Comment on the morphology of the erythrocytes.
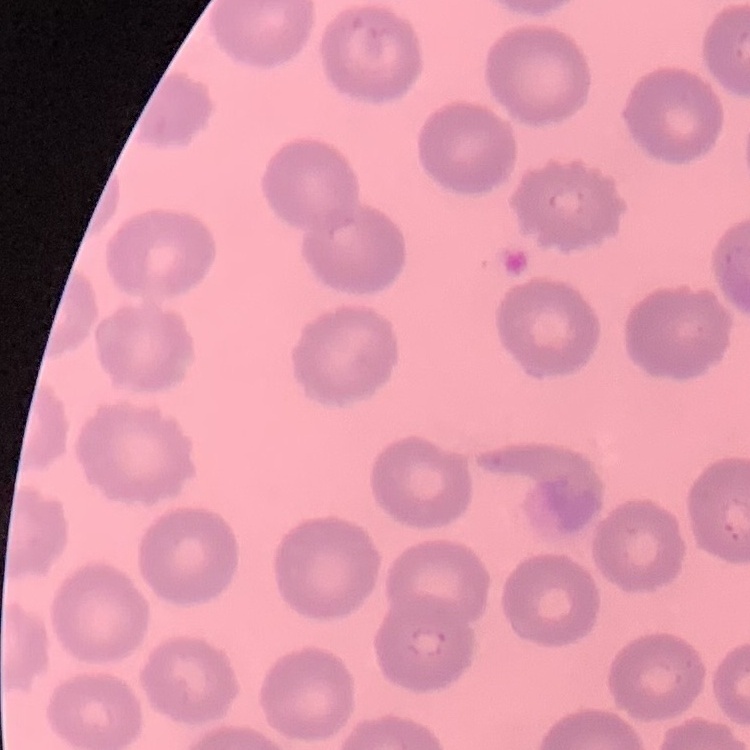

They show no rouleaux formation.

Summary:
  - Stain: Field's or Giemsa
  - Preparation: thin blood film
  - Image type: one tile cut from a larger photomicrograph